Outline each blood parasite and name the species.
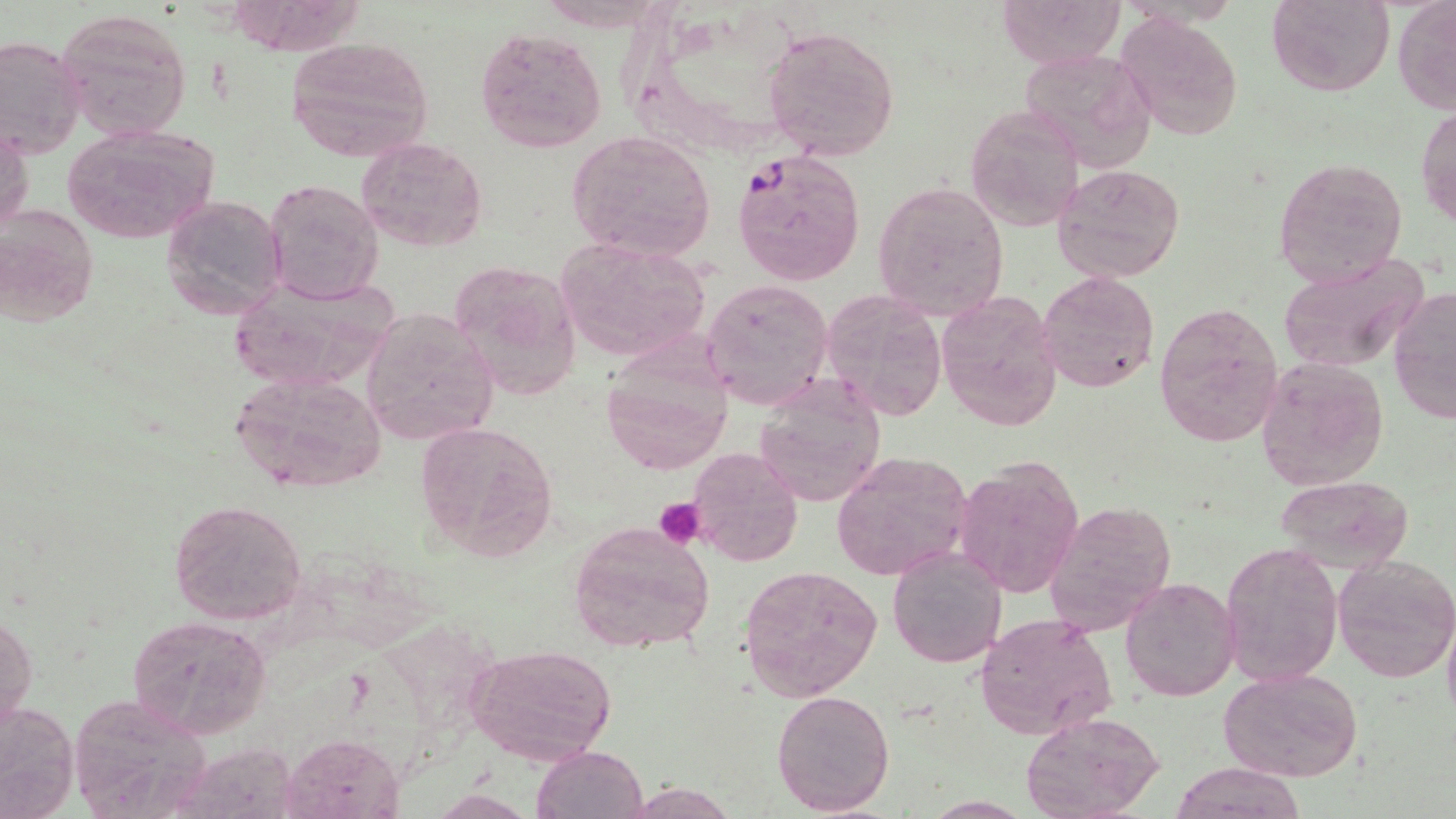
Approximate bounding boxes as [x1, y1, x2, y2] in pixels.
Plasmodium falciparum-infected red blood cells: [732, 147, 865, 289].
No Plasmodium ovale, Plasmodium malariae, Plasmodium vivax, Babesia divergens, or Trypanosoma brucei observed.

slide-level diagnosis = Plasmodium falciparum
platelet locations = approximate bounding boxes as [x1, y1, x2, y2] in pixels: [653, 498, 707, 549]
uninfected red blood cell locations = approximate bounding boxes as [x1, y1, x2, y2] in pixels: [1000, 0, 1123, 69], [1267, 0, 1394, 97], [1392, 0, 1456, 116], [57, 9, 192, 139], [1116, 10, 1244, 142], [762, 25, 899, 160], [474, 26, 607, 153], [0, 33, 86, 162], [284, 35, 435, 164], [1019, 47, 1159, 173], [983, 77, 1123, 199], [964, 103, 1085, 234], [1416, 104, 1456, 228], [1, 124, 33, 241], [61, 124, 219, 244], [566, 130, 716, 264], [356, 136, 488, 253], [1273, 159, 1407, 287], [1053, 164, 1185, 282], [263, 179, 384, 304], [871, 181, 1009, 322], [161, 193, 288, 321], [0, 204, 98, 327], [555, 237, 710, 361], [1276, 251, 1431, 373], [450, 260, 583, 400], [1036, 270, 1159, 392], [224, 274, 401, 393], [702, 278, 835, 412], [1388, 288, 1455, 424], [822, 289, 948, 419], [937, 292, 1063, 435], [1154, 301, 1285, 446], [360, 307, 499, 448], [599, 344, 734, 477], [1255, 356, 1390, 491], [226, 370, 387, 498], [752, 377, 888, 508], [414, 420, 557, 563], [686, 447, 805, 567], [831, 452, 972, 581], [953, 458, 1086, 599], [1277, 475, 1412, 571], [168, 498, 307, 626], [1044, 498, 1176, 635], [568, 520, 716, 655], [1220, 541, 1343, 688], [887, 547, 1007, 668], [1331, 555, 1456, 683], [737, 564, 882, 700], [1120, 576, 1239, 701], [1442, 608, 1456, 732], [1, 613, 36, 732], [129, 614, 271, 741], [973, 614, 1117, 740], [463, 643, 618, 766], [1218, 668, 1362, 783], [71, 688, 216, 816], [770, 688, 895, 816], [0, 699, 78, 817], [1021, 713, 1165, 819], [280, 734, 405, 819], [184, 739, 308, 819], [532, 746, 649, 819], [1169, 763, 1308, 819], [627, 781, 735, 818], [431, 792, 536, 819]
field of view = single
magnification = 1000x
stain = May-Grünwald-Giemsa
preparation = thin blood smear
image size = 1456×819 pixels
modality = light microscopy